Locate and identify every blood parasite.
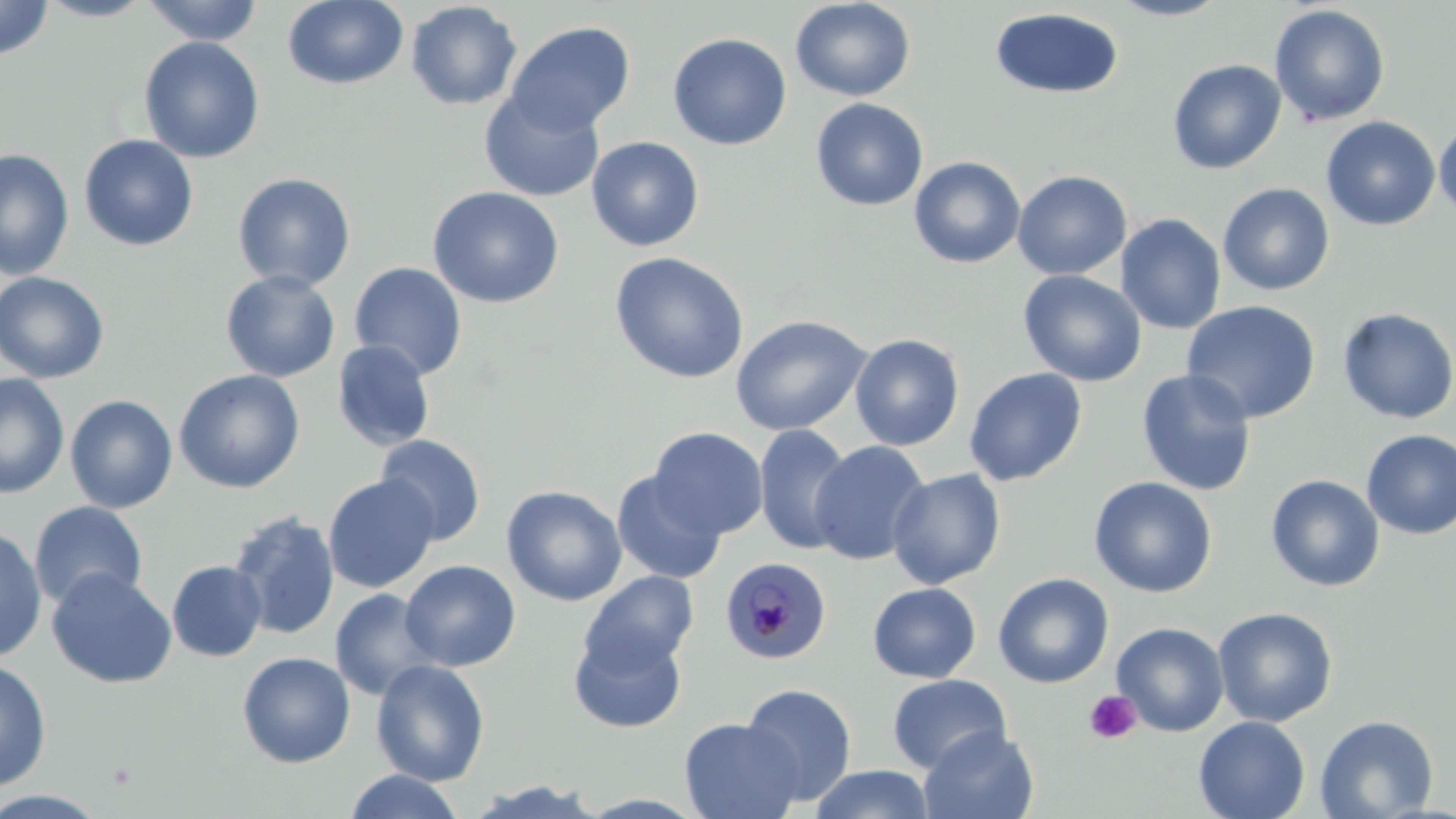

Approximate bounding boxes as (x1,y1)-(x2,y2) corner pairs in pixels.
Plasmodium malariae-infected red blood cells: (719,556)-(832,664).
No Plasmodium falciparum, Plasmodium ovale, Plasmodium vivax, Babesia divergens, or Trypanosoma brucei observed.

Platelet locations: (1083,690)-(1142,744). Uninfected red blood cell locations: (0,0)-(54,60), (37,0)-(155,22), (141,0)-(263,45), (282,0)-(409,90), (791,0)-(915,102), (1107,0)-(1232,21), (405,1)-(523,110), (1269,4)-(1391,127), (989,7)-(1124,99), (505,21)-(636,135), (667,32)-(792,150), (138,36)-(265,163), (1167,59)-(1286,175), (479,89)-(605,202), (810,98)-(928,211), (1321,116)-(1441,231), (1434,118)-(1456,222), (79,134)-(199,251), (586,135)-(705,252), (0,148)-(75,279), (909,155)-(1026,269), (1012,169)-(1132,280), (232,172)-(356,291), (1218,183)-(1335,296), (426,186)-(564,308), (1116,214)-(1226,334), (609,252)-(749,384), (349,262)-(468,380), (1018,269)-(1147,387), (221,270)-(340,382), (0,271)-(110,384), (1181,300)-(1321,422), (1337,307)-(1456,425), (730,315)-(871,436), (850,333)-(965,451), (332,340)-(436,451), (964,367)-(1088,487), (1136,368)-(1258,496), (173,369)-(305,493), (0,373)-(70,498), (65,394)-(178,513), (753,424)-(854,555), (649,426)-(769,539), (1361,429)-(1456,539), (375,434)-(486,546), (809,440)-(930,565), (887,468)-(1006,589), (611,470)-(727,584), (323,474)-(440,593), (1265,474)-(1385,592), (1088,477)-(1217,598), (501,485)-(627,606), (29,501)-(148,610), (227,509)-(340,640), (0,525)-(47,663), (166,560)-(268,662), (399,560)-(520,672), (46,567)-(177,689), (580,570)-(699,674), (993,572)-(1114,688), (867,581)-(981,684), (329,587)-(441,701), (1212,606)-(1338,727), (1111,622)-(1230,736), (569,627)-(686,734), (237,651)-(356,768), (0,657)-(53,791), (370,659)-(491,786), (887,673)-(1011,774), (740,682)-(857,805), (1314,714)-(1439,819), (1193,715)-(1310,819), (679,717)-(804,819), (919,726)-(1038,819), (809,764)-(935,819), (342,770)-(466,819), (463,779)-(610,818), (0,789)-(111,818). Slide-level diagnosis: Plasmodium malariae. Thin blood film. May-Grünwald-Giemsa-stained preparation. One field of a larger specimen. 1000x magnification. Image is 1456×819 pixels. Optical microscopy.